Comment on the morphology of the erythrocytes.
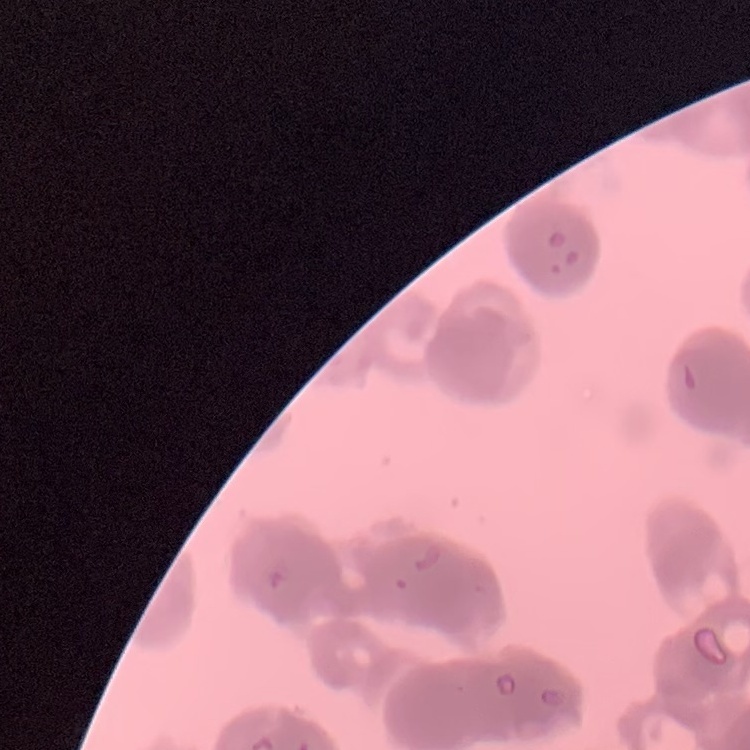

Rouleaux formation.

Stained with either Field's or Giemsa. Thin blood smear. Square crop of a larger photomicrograph.